Classify this cell by malaria status.
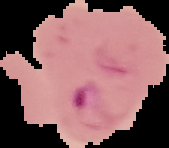

Parasitized.

Summary:
  - Preparation: thin blood film
  - Image type: segmented cell region on a black background
  - Image size: 169×148 pixels